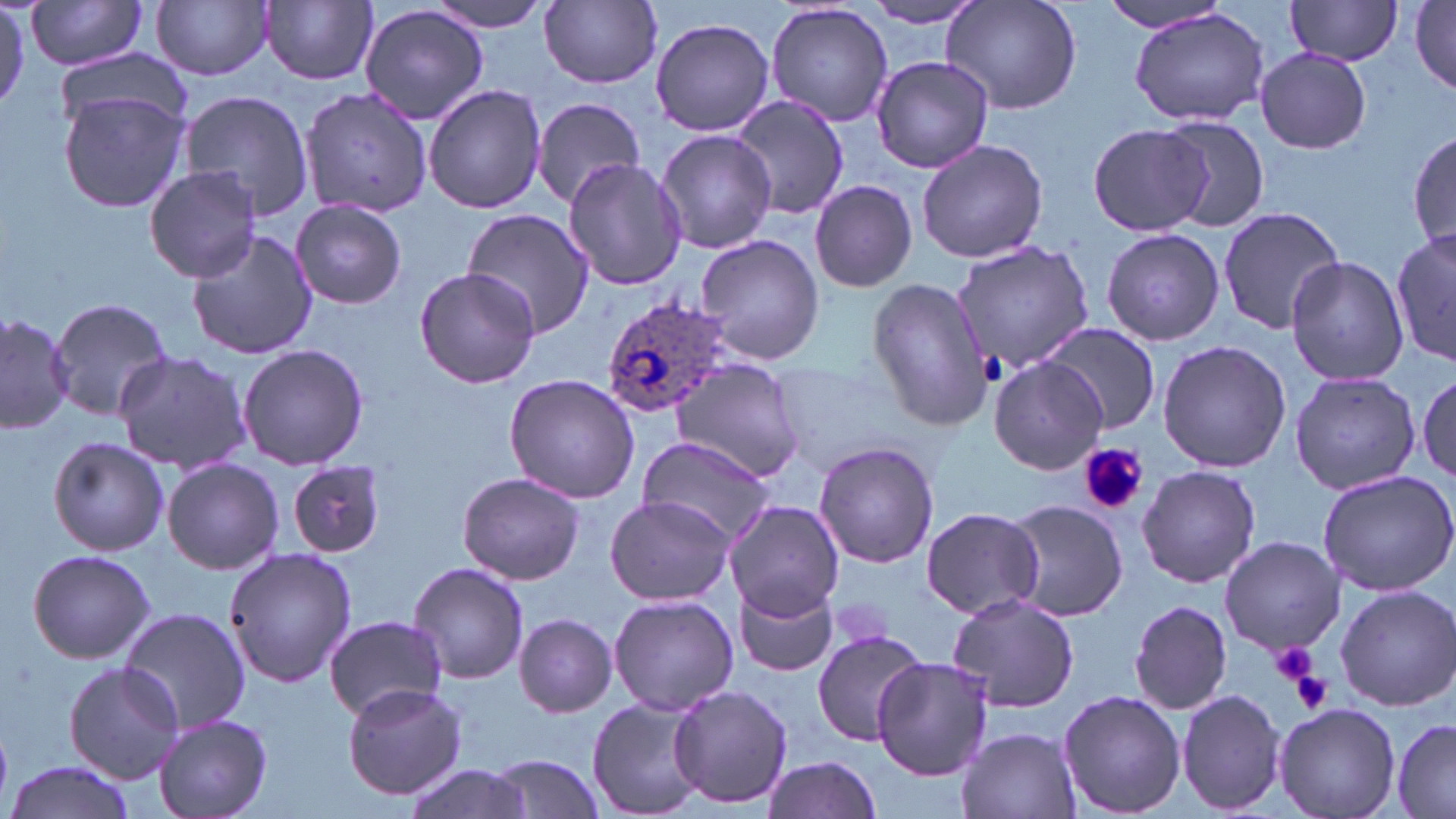

Summary:
  - Coordinate format: approximate bounding boxes as (x1,y1)-(x2,y2) corner pairs in pixels
  - Platelet locations: (1079,443)-(1148,515), (1267,641)-(1320,685), (1291,670)-(1335,713)
  - Uninfected red blood cell locations: (23,0)-(153,70), (152,0)-(274,81), (421,0)-(557,33), (260,1)-(378,86), (540,1)-(662,87), (862,1)-(989,26), (943,1)-(1081,115), (1409,1)-(1456,93), (1094,2)-(1234,33), (1284,2)-(1403,67), (360,4)-(489,125), (766,4)-(893,127), (1128,8)-(1270,128), (649,16)-(775,136), (1255,47)-(1371,154), (50,50)-(191,140), (870,55)-(993,172), (423,84)-(548,213), (300,85)-(432,217), (58,87)-(190,212), (181,92)-(314,217), (729,95)-(848,222), (531,97)-(646,203), (1158,115)-(1271,232), (1087,122)-(1212,238), (656,129)-(775,254), (1409,129)-(1456,252), (916,138)-(1048,263), (562,158)-(689,290), (143,166)-(261,281), (809,181)-(917,293), (291,199)-(407,310), (461,207)-(596,340), (1217,207)-(1348,334), (1101,227)-(1224,347), (185,228)-(318,361), (1390,228)-(1455,367), (695,235)-(826,366), (952,241)-(1095,370), (1285,255)-(1411,388), (414,265)-(541,389), (865,279)-(993,430), (47,296)-(174,422), (0,311)-(73,434), (1039,323)-(1161,435), (1155,340)-(1292,472), (237,344)-(369,470), (114,351)-(252,474), (990,357)-(1106,476), (670,358)-(808,483), (1412,367)-(1456,489), (1289,370)-(1422,498), (503,372)-(644,503), (48,435)-(170,556), (635,435)-(780,548), (813,442)-(940,569), (162,458)-(284,574), (287,459)-(387,558), (1136,464)-(1260,591), (1317,469)-(1456,596), (456,472)-(586,585), (605,496)-(735,606), (1001,498)-(1129,621), (726,501)-(844,618), (918,507)-(1044,620), (1218,535)-(1347,655), (224,547)-(357,689), (26,548)-(156,665), (407,561)-(529,684), (734,583)-(839,677), (1334,584)-(1456,711), (609,593)-(739,717), (947,593)-(1080,714), (1128,600)-(1236,716), (118,607)-(253,733), (514,614)-(617,716), (324,615)-(448,721), (811,629)-(926,745), (870,655)-(993,781), (64,663)-(186,784), (342,684)-(469,801), (667,685)-(794,808), (1057,688)-(1186,818), (1176,688)-(1286,815), (586,698)-(706,816), (1274,702)-(1399,819), (154,714)-(271,818), (1391,715)-(1456,819), (955,726)-(1081,819), (489,755)-(606,819), (759,756)-(883,819), (4,758)-(137,819), (400,760)-(533,819)
  - Plasmodium ovale-infected red blood cell locations: (602,297)-(734,420)
  - Slide-level diagnosis: Plasmodium ovale
  - Stain: May-Grünwald-Giemsa
  - Modality: optical microscopy
  - Image size: 1456×819 pixels
  - Field of view: single
  - Magnification: 1000x
  - Preparation: thin blood smear